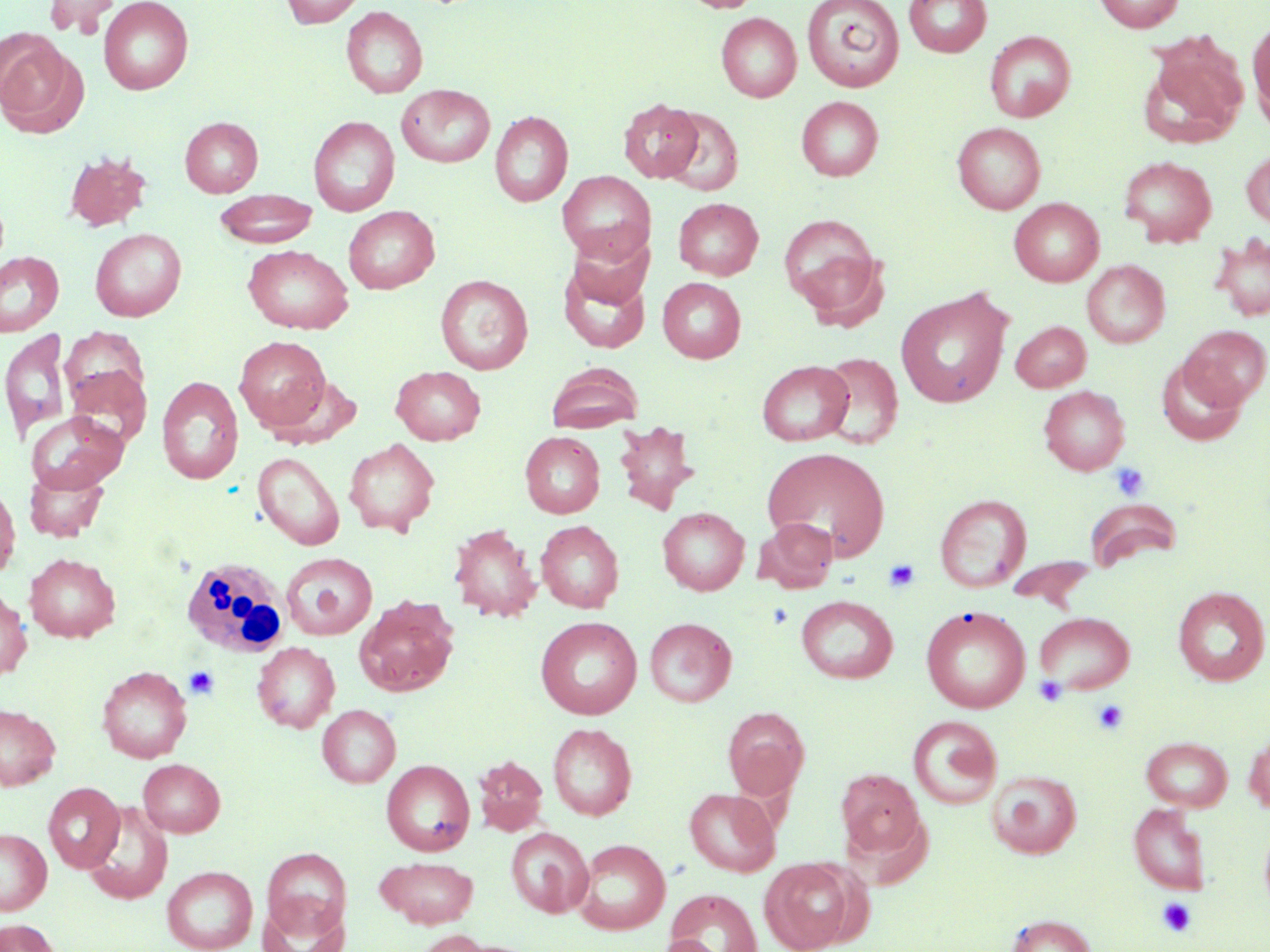

{
  "slide_level_diagnosis": "negative for blood parasites",
  "field_of_view": "single",
  "white_blood_cell_locations": "approximate bounding boxes as named x1/y1/x2/y2 corners in pixels: (x1=179, y1=556, x2=290, y2=659)",
  "image_size": "1270×952 pixels",
  "stain": "May-Grünwald-Giemsa",
  "preparation": "thin blood film",
  "platelet_locations": "approximate bounding boxes as named x1/y1/x2/y2 corners in pixels: (x1=1110, y1=463, x2=1149, y2=501), (x1=884, y1=558, x2=921, y2=592), (x1=185, y1=665, x2=219, y2=699), (x1=1033, y1=675, x2=1068, y2=707), (x1=1092, y1=699, x2=1128, y2=735), (x1=1156, y1=897, x2=1196, y2=937)",
  "modality": "light microscopy",
  "magnification": "1000x",
  "uninfected_red_blood_cell_locations": "approximate bounding boxes as named x1/y1/x2/y2 corners in pixels: (x1=44, y1=0, x2=120, y2=36), (x1=99, y1=0, x2=193, y2=94), (x1=281, y1=0, x2=366, y2=28), (x1=678, y1=0, x2=765, y2=13), (x1=802, y1=0, x2=904, y2=91), (x1=903, y1=0, x2=992, y2=57), (x1=1093, y1=0, x2=1185, y2=32), (x1=341, y1=6, x2=428, y2=98), (x1=716, y1=12, x2=802, y2=102), (x1=1248, y1=19, x2=1270, y2=126), (x1=985, y1=30, x2=1076, y2=122), (x1=0, y1=37, x2=83, y2=137), (x1=1139, y1=44, x2=1247, y2=149), (x1=397, y1=84, x2=495, y2=168), (x1=797, y1=96, x2=883, y2=181), (x1=618, y1=98, x2=703, y2=183), (x1=660, y1=108, x2=743, y2=195), (x1=490, y1=110, x2=573, y2=207), (x1=180, y1=116, x2=263, y2=197), (x1=308, y1=116, x2=400, y2=216), (x1=952, y1=122, x2=1046, y2=214), (x1=1242, y1=148, x2=1270, y2=230), (x1=63, y1=151, x2=152, y2=232), (x1=1119, y1=156, x2=1217, y2=246), (x1=557, y1=170, x2=655, y2=264), (x1=214, y1=189, x2=317, y2=248), (x1=673, y1=197, x2=764, y2=279), (x1=1009, y1=198, x2=1104, y2=286), (x1=344, y1=206, x2=440, y2=294), (x1=779, y1=213, x2=885, y2=320), (x1=566, y1=227, x2=653, y2=310), (x1=90, y1=228, x2=186, y2=321), (x1=1210, y1=233, x2=1270, y2=322), (x1=242, y1=244, x2=354, y2=334), (x1=0, y1=251, x2=64, y2=336), (x1=558, y1=259, x2=651, y2=353), (x1=1082, y1=260, x2=1170, y2=347), (x1=435, y1=275, x2=533, y2=374), (x1=658, y1=277, x2=746, y2=363), (x1=896, y1=288, x2=1012, y2=408), (x1=1011, y1=321, x2=1091, y2=391), (x1=1181, y1=324, x2=1269, y2=409), (x1=61, y1=328, x2=150, y2=417), (x1=0, y1=329, x2=70, y2=443), (x1=234, y1=336, x2=331, y2=431), (x1=817, y1=352, x2=903, y2=448), (x1=1155, y1=357, x2=1248, y2=446), (x1=757, y1=360, x2=854, y2=446), (x1=547, y1=363, x2=643, y2=432), (x1=63, y1=364, x2=152, y2=450), (x1=390, y1=365, x2=485, y2=444), (x1=156, y1=376, x2=244, y2=484), (x1=1038, y1=386, x2=1130, y2=475), (x1=26, y1=411, x2=128, y2=494), (x1=613, y1=419, x2=700, y2=516), (x1=520, y1=432, x2=605, y2=518), (x1=344, y1=437, x2=440, y2=536), (x1=761, y1=446, x2=891, y2=560), (x1=253, y1=452, x2=344, y2=550), (x1=24, y1=465, x2=109, y2=542), (x1=0, y1=480, x2=19, y2=581), (x1=935, y1=494, x2=1031, y2=593), (x1=1085, y1=499, x2=1182, y2=572), (x1=657, y1=507, x2=749, y2=595), (x1=755, y1=517, x2=839, y2=592), (x1=536, y1=520, x2=624, y2=613), (x1=448, y1=523, x2=541, y2=622), (x1=25, y1=552, x2=120, y2=642), (x1=281, y1=552, x2=377, y2=640), (x1=1007, y1=556, x2=1097, y2=609), (x1=1173, y1=587, x2=1269, y2=685), (x1=0, y1=589, x2=31, y2=681), (x1=796, y1=594, x2=898, y2=683), (x1=354, y1=595, x2=459, y2=696), (x1=921, y1=606, x2=1031, y2=714), (x1=1034, y1=611, x2=1135, y2=693), (x1=535, y1=616, x2=642, y2=719), (x1=645, y1=617, x2=736, y2=706), (x1=252, y1=641, x2=340, y2=733), (x1=97, y1=665, x2=193, y2=763), (x1=0, y1=704, x2=61, y2=790), (x1=317, y1=704, x2=401, y2=787), (x1=723, y1=707, x2=810, y2=799), (x1=908, y1=716, x2=1002, y2=809), (x1=547, y1=723, x2=637, y2=820), (x1=1244, y1=731, x2=1270, y2=814), (x1=1141, y1=736, x2=1233, y2=811), (x1=474, y1=756, x2=548, y2=835), (x1=138, y1=758, x2=225, y2=837), (x1=381, y1=759, x2=474, y2=856), (x1=836, y1=768, x2=926, y2=861), (x1=988, y1=769, x2=1081, y2=858), (x1=43, y1=782, x2=124, y2=873), (x1=684, y1=787, x2=781, y2=877), (x1=82, y1=802, x2=173, y2=905), (x1=1129, y1=803, x2=1211, y2=894), (x1=506, y1=827, x2=593, y2=917), (x1=0, y1=828, x2=51, y2=915), (x1=574, y1=838, x2=670, y2=934), (x1=261, y1=847, x2=352, y2=938), (x1=375, y1=856, x2=479, y2=928), (x1=760, y1=858, x2=857, y2=951), (x1=162, y1=865, x2=258, y2=951), (x1=666, y1=889, x2=763, y2=952), (x1=259, y1=898, x2=348, y2=952), (x1=1006, y1=914, x2=1097, y2=952), (x1=0, y1=919, x2=60, y2=952), (x1=410, y1=930, x2=494, y2=952), (x1=655, y1=936, x2=726, y2=952)"
}